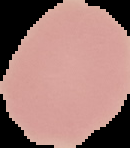
preparation = thin blood smear
image type = segmented cell region on a black background
result = negative for malaria parasites
image size = 130×148 pixels